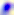

modality = micrograph
magnification = 400x
identification = Toxoplasma gondii